Assess this cell for malaria.
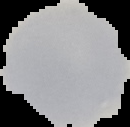

Uninfected.

preparation = thin blood film
image size = 130×127 pixels
image type = segmented cell region with the area outside set to black